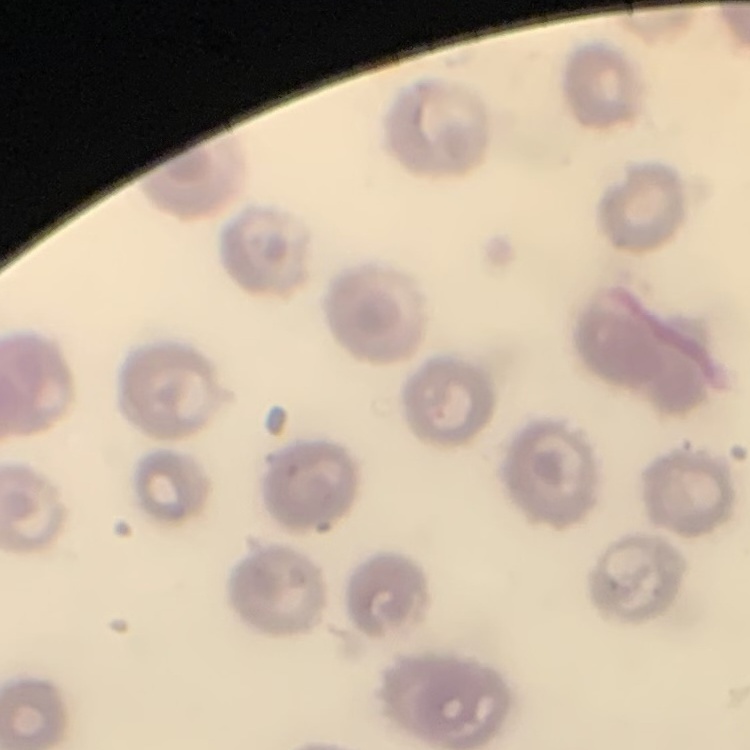
Summary:
  - Red blood cell morphology: no rouleaux formation
  - Stain: Field's or Giemsa
  - Image type: square crop of a larger photomicrograph
  - Preparation: thin peripheral smear